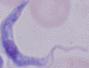

Summary:
  - Modality: photomicrograph
  - Identification: trypanosome
  - Magnification: 1000x